Assess the morphology of the red blood cells.
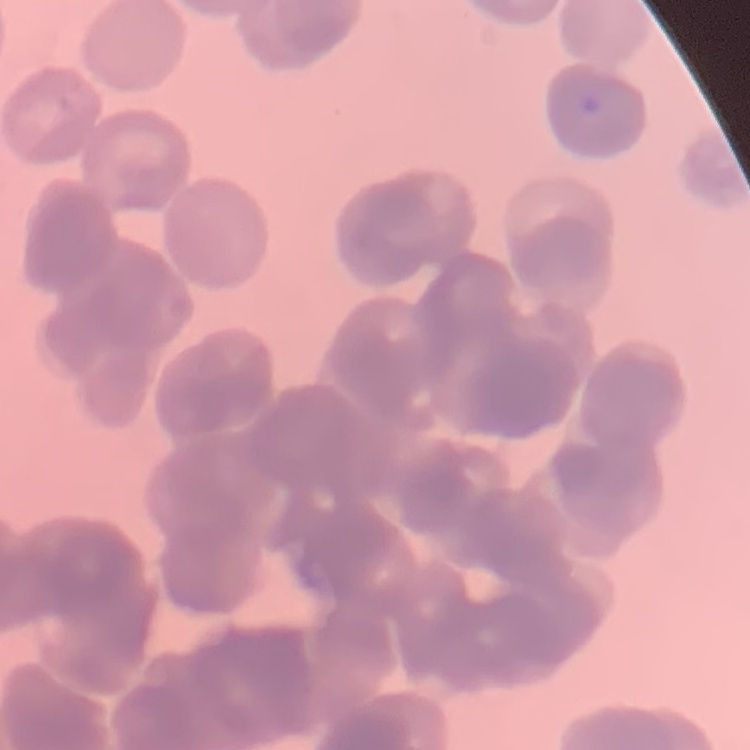
They show rouleaux formation.

One tile cut from a larger photomicrograph. Stained with either Field's or Giemsa. Thin peripheral smear.